Report the malaria status of this cell.
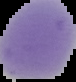

It is uninfected.

From a thin blood film. Image is 76×82 pixels. Cell region segmented out of the field of view; the surrounding area is masked to black.